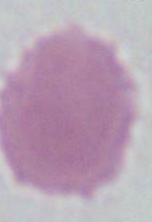
{
  "modality": "photomicrograph",
  "identification": "red blood cell",
  "magnification": "1000x"
}